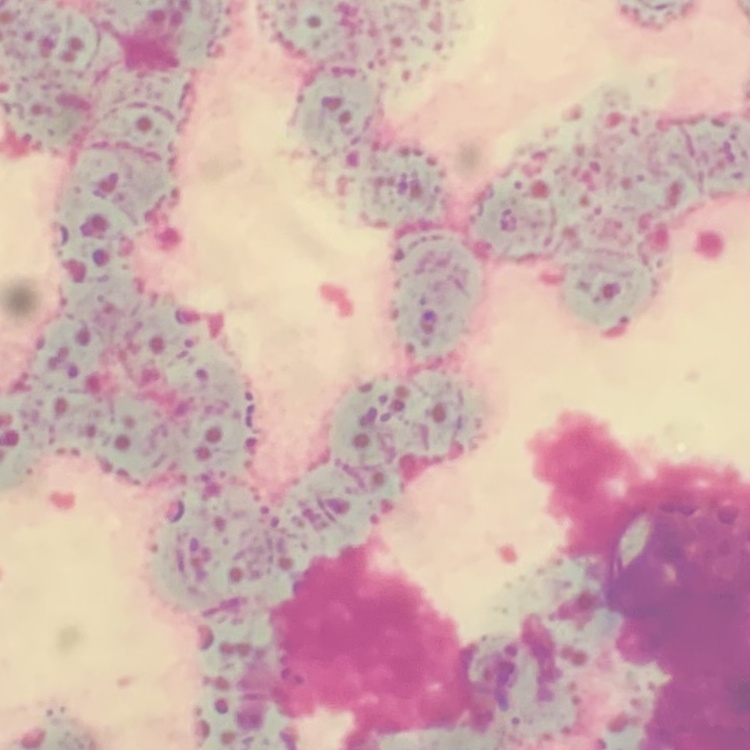
Summary:
  - Erythrocyte morphology: rouleaux formation
  - Preparation: thin blood film
  - Stain: Field's or Giemsa
  - Image type: one tile cut from a larger photomicrograph